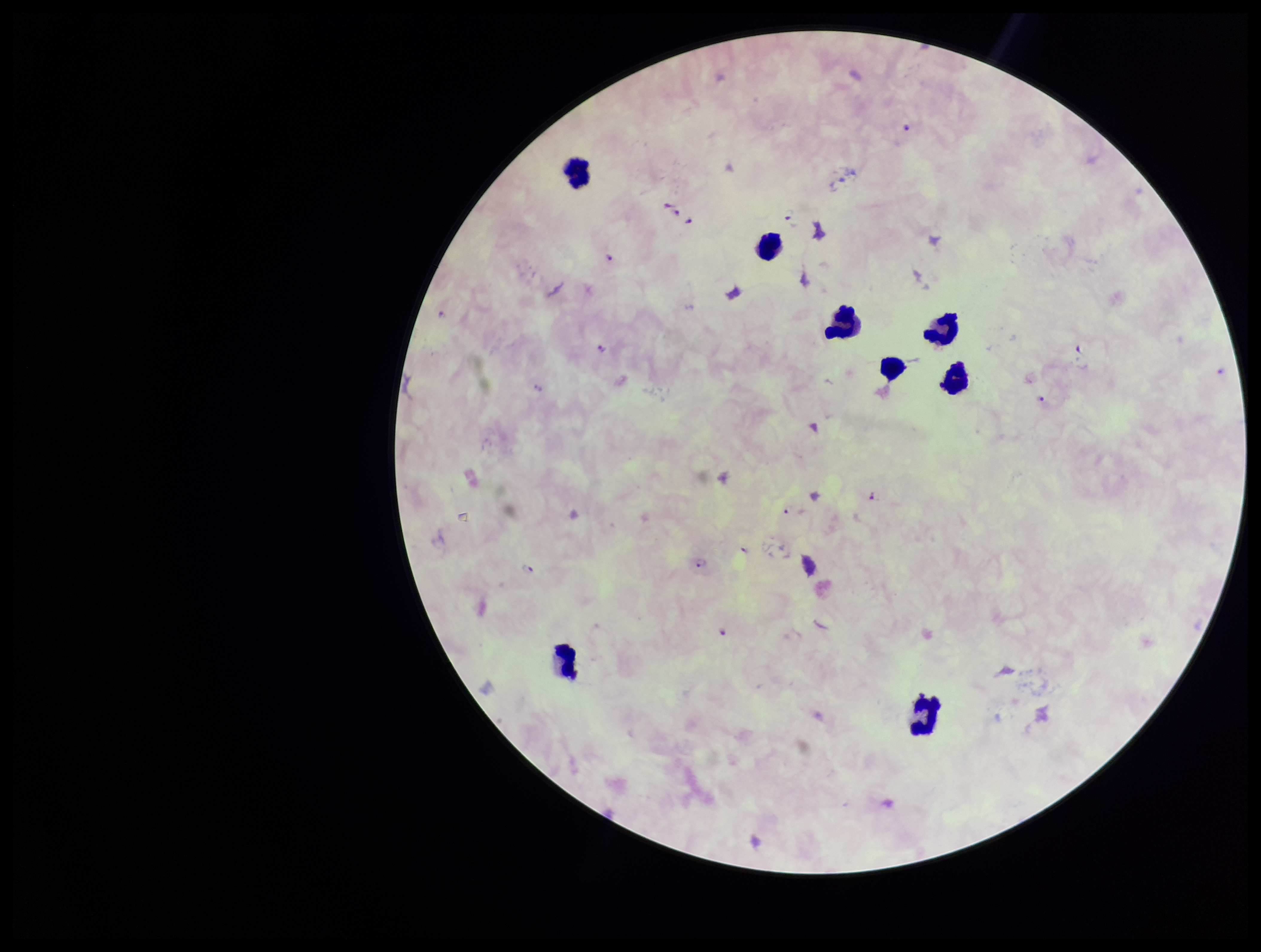

Leukocyte count: 8. Parasite count: 14. Image is 1261×952 pixels. Photographed through the microscope eyepiece with a smartphone camera. Preparation: thick smear. Stained with Giemsa. One field from this slide. Plasmodium parasites: seen. Patient malaria status: positive. Species reported for this patient: Plasmodium falciparum.